Identify the preparation type.
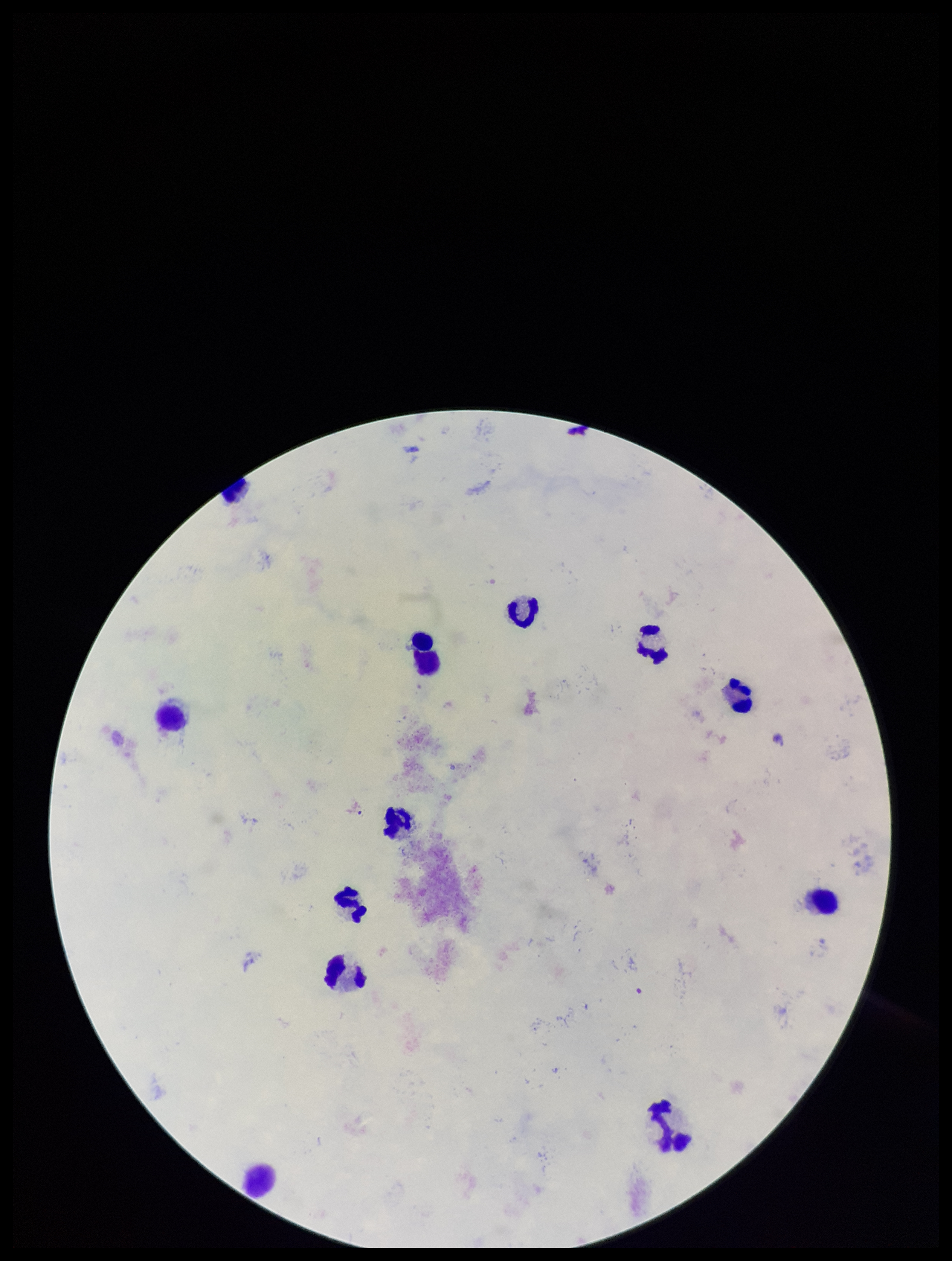
A thick smear.

{
  "field_of_view": "one from this slide",
  "parasite_count": 0,
  "capture": "smartphone photograph through the microscope eyepiece",
  "patient_malaria_status": "negative",
  "image_size": "952×1261 pixels",
  "stain": "Giemsa",
  "plasmodium_parasites": "none detected",
  "leukocyte_count": 12
}